Classify this cell by malaria status.
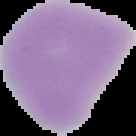

Uninfected.

Summary:
  - Image size: 136×136 pixels
  - Preparation: thin blood film
  - Image type: segmented cell region with the area outside set to black